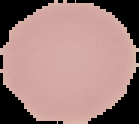

Summary:
  - Image size: 139×124 pixels
  - Preparation: thin blood film
  - Image type: segmented cell region on a black background
  - Malaria status: uninfected